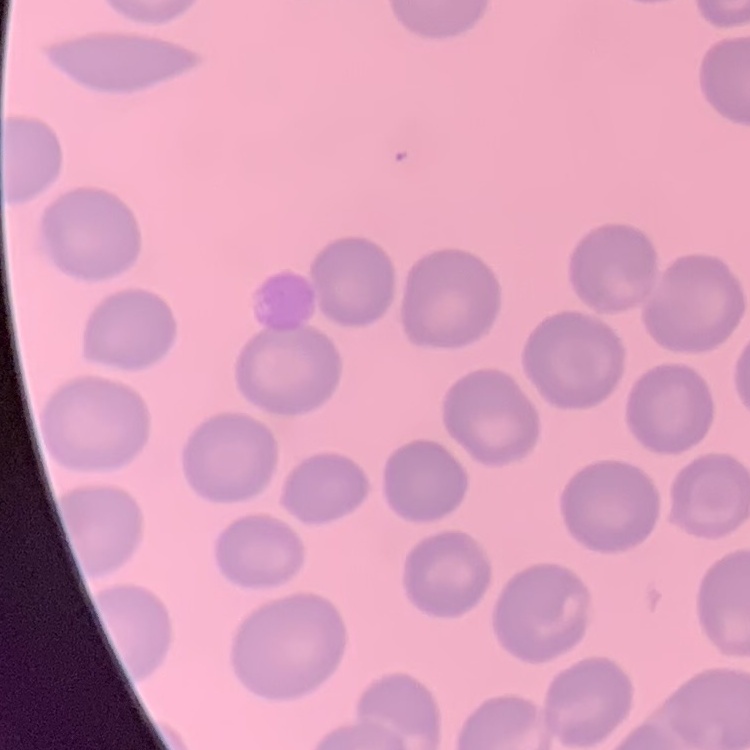

erythrocyte morphology = no rouleaux formation
preparation = thin peripheral smear
stain = Field's or Giemsa
image type = one tile cut from a larger photomicrograph